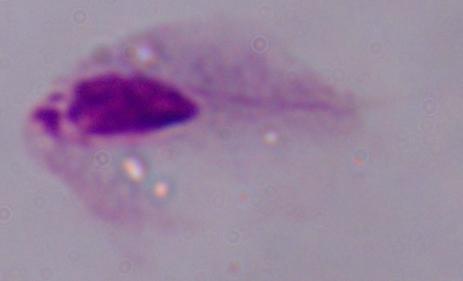
identification = trichomonad
modality = photomicrograph
magnification = 1000x